Comment on the morphology of the erythrocytes.
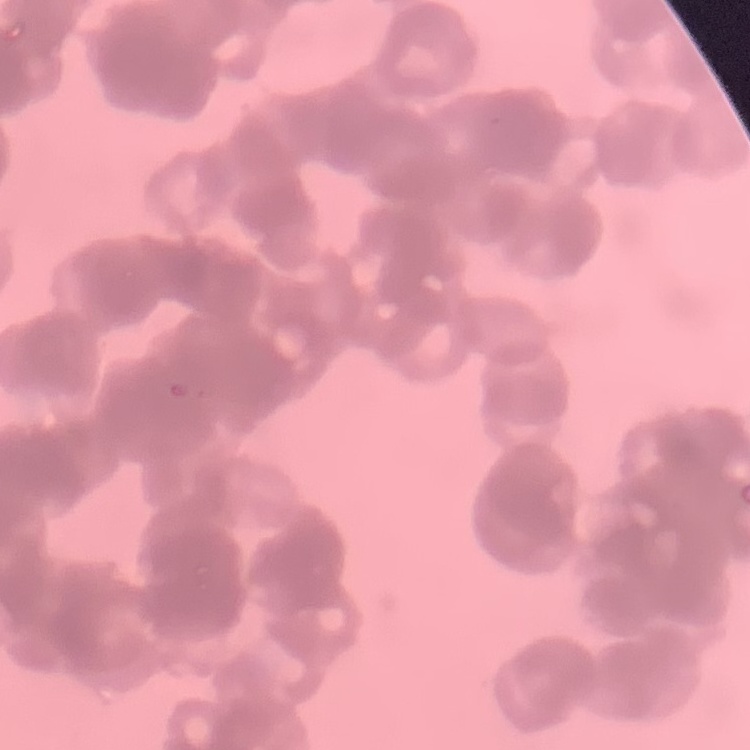
Rouleaux formation.

Summary:
  - Stain: Field's or Giemsa
  - Image type: square crop of a larger photomicrograph
  - Preparation: thin peripheral smear